Assess the morphology of the red blood cells.
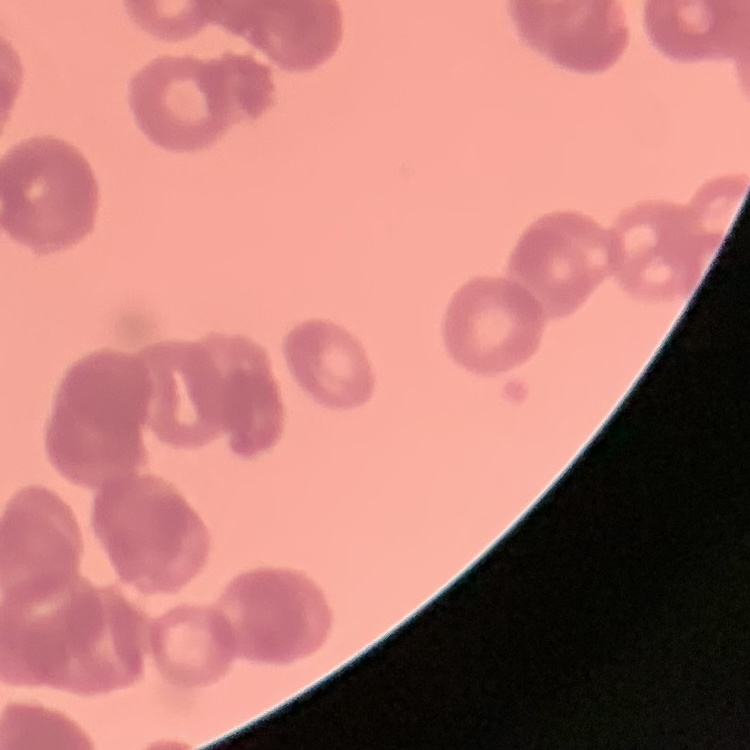

They show rouleaux formation.

stain = Field's or Giemsa
image type = one tile cut from a larger photomicrograph
preparation = thin peripheral smear